Name the parasite shown.
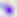

This is Toxoplasma gondii.

{
  "modality": "photomicrograph",
  "magnification": "400x"
}